Outline each Plasmodium falciparum parasite and classify it by life-cycle stage.
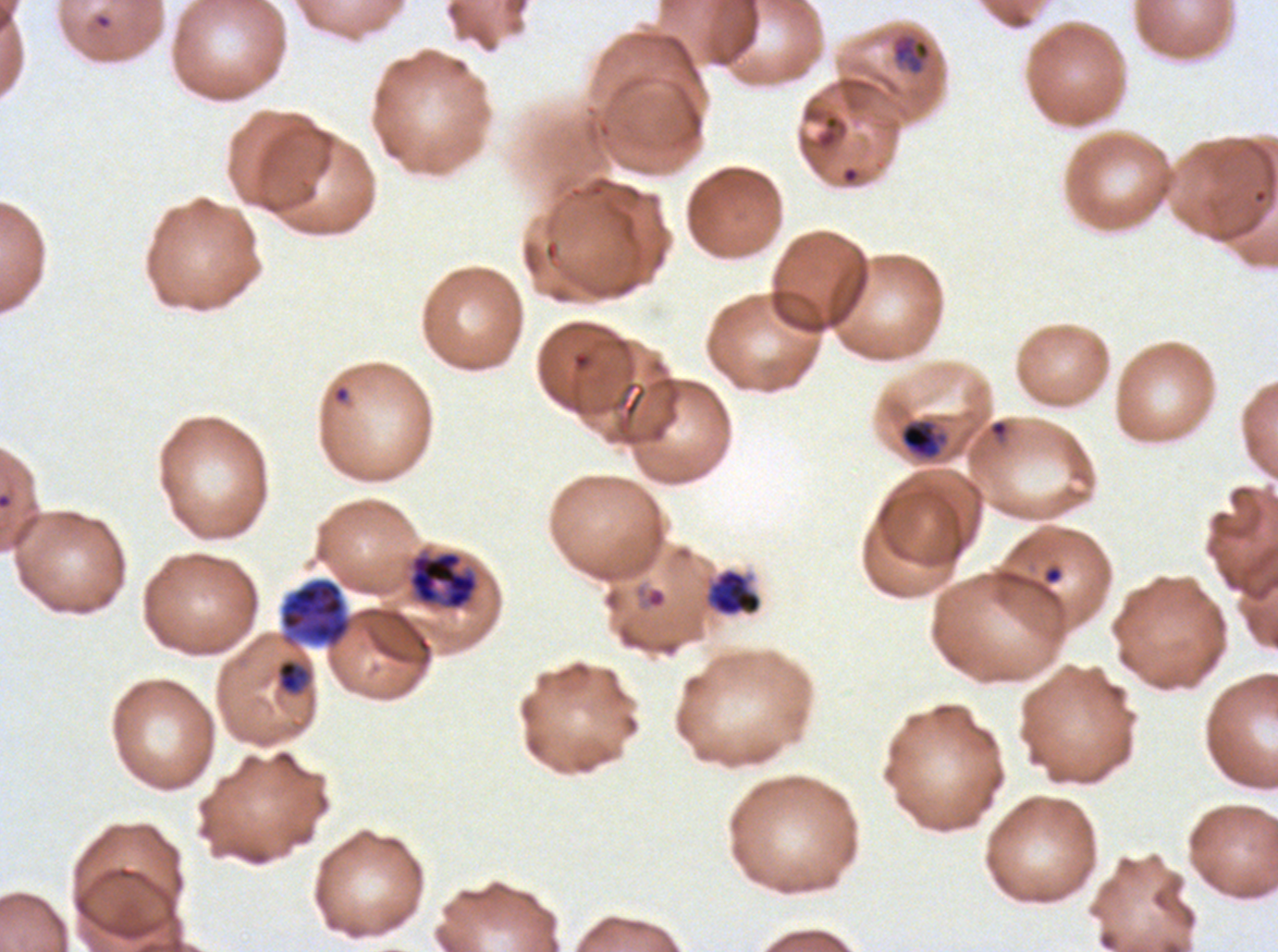
Approximate bounding rectangles given as corner coordinates in pixels from the top-left.
Rings: (x1=94, y1=14, x2=111, y2=29), (x1=332, y1=384, x2=350, y2=405), (x1=1042, y1=565, x2=1063, y2=585), (x1=633, y1=585, x2=669, y2=611).
Late-ring/early-trophozoite forms: (x1=891, y1=35, x2=931, y2=74), (x1=899, y1=419, x2=948, y2=460), (x1=276, y1=659, x2=310, y2=694).
Early schizonts: (x1=408, y1=551, x2=479, y2=610), (x1=279, y1=577, x2=352, y2=648).
No mid trophozoites, late trophozoites, late schizonts, segmenters, or gametocytes observed.

Debris locations: (x1=704, y1=567, x2=763, y2=617). Thin blood film. Image is 1278×952 pixels. One sub-image of a larger composite. Giemsa stain. Ex-vivo Plasmodium falciparum culture from a patient in The Gambia, grown for 24 to 48 hours. Life-cycle stages observed: ring, late-ring/early-trophozoite, early schizont.